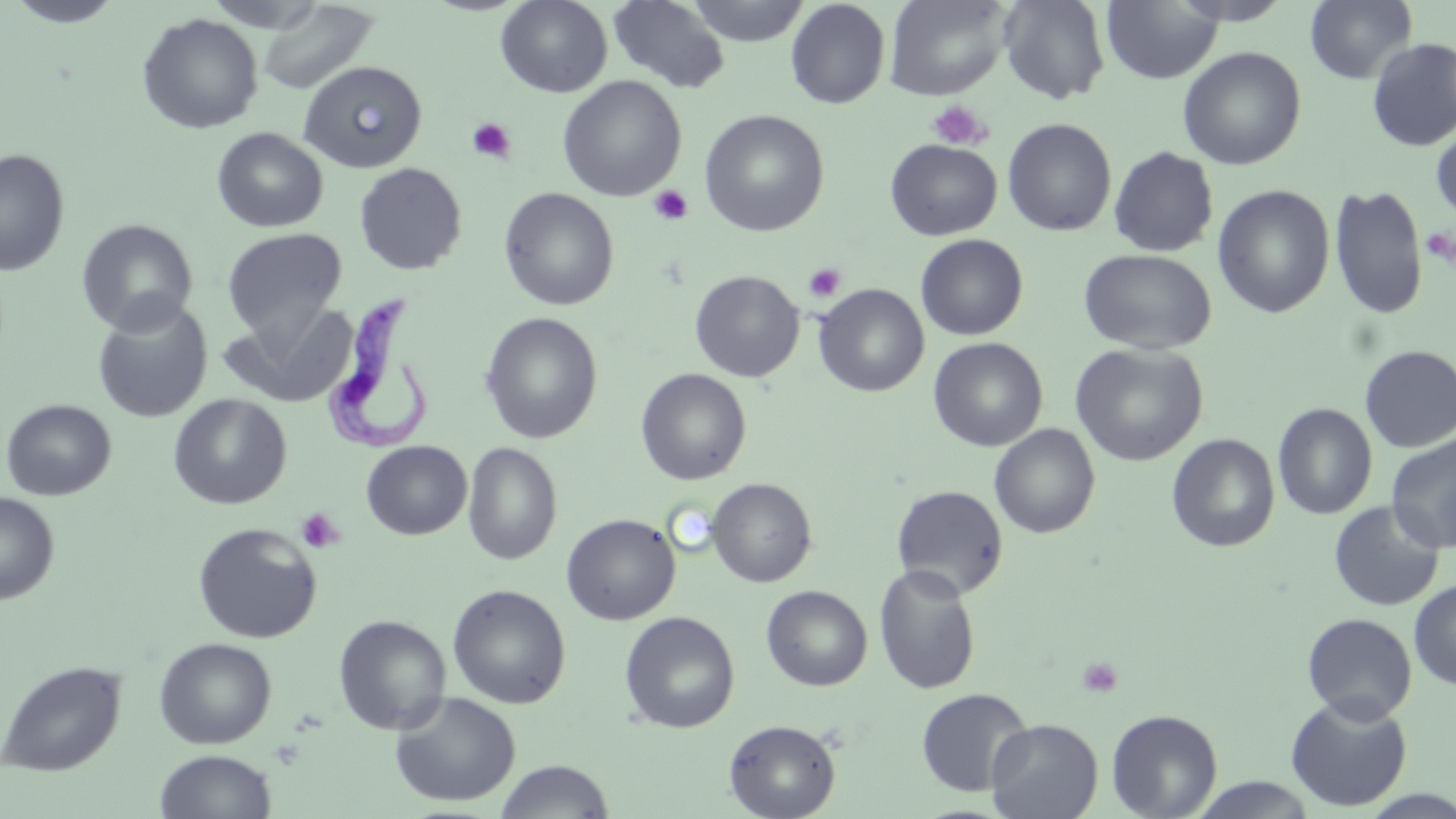
slide-level diagnosis = Trypanosoma brucei
uninfected red blood cell locations = approximate bounding boxes as (x1, y1, x2, y2) in pixels: (4, 0, 129, 28), (495, 0, 613, 98), (685, 0, 810, 46), (785, 0, 891, 109), (883, 0, 1012, 100), (997, 0, 1111, 105), (1101, 0, 1222, 84), (1303, 0, 1418, 85), (606, 1, 731, 94), (255, 2, 381, 96), (137, 13, 263, 134), (1366, 38, 1456, 152), (1177, 46, 1307, 170), (298, 61, 427, 173), (557, 75, 686, 202), (699, 109, 829, 237), (1002, 118, 1117, 236), (1430, 121, 1456, 225), (211, 127, 328, 232), (885, 139, 1002, 241), (1108, 146, 1219, 257), (0, 148, 70, 276), (354, 163, 467, 275), (1328, 183, 1428, 320), (1212, 185, 1335, 318), (498, 187, 619, 311), (76, 218, 198, 336), (221, 227, 347, 341), (915, 234, 1028, 340), (1078, 248, 1217, 355), (689, 270, 805, 382), (814, 284, 929, 397), (92, 298, 213, 423), (219, 300, 359, 409), (480, 312, 603, 444), (928, 337, 1048, 452), (1070, 342, 1209, 466), (1359, 344, 1456, 453), (635, 368, 752, 485), (169, 394, 292, 509), (1, 398, 117, 501), (1272, 402, 1378, 519), (989, 423, 1100, 539), (1166, 433, 1280, 553), (1386, 434, 1456, 553), (361, 441, 471, 540), (462, 442, 562, 566), (706, 478, 817, 587), (891, 484, 1009, 598), (0, 492, 59, 604), (1328, 500, 1446, 612), (561, 513, 680, 625), (192, 522, 323, 644), (873, 564, 981, 695), (1409, 580, 1456, 690), (447, 583, 571, 709), (761, 585, 872, 691), (619, 610, 740, 733), (1302, 613, 1417, 723), (333, 615, 452, 735), (154, 637, 277, 749), (0, 659, 127, 777), (915, 687, 1034, 796), (389, 692, 521, 808), (1285, 695, 1413, 812), (1105, 708, 1223, 819), (986, 717, 1103, 818), (724, 719, 841, 819), (154, 749, 277, 819), (494, 759, 615, 818), (1188, 777, 1319, 818)
Trypanosoma brucei locations = approximate bounding boxes as (x1, y1, x2, y2) in pixels: (315, 298, 435, 452)
field of view = single
platelet locations = approximate bounding boxes as (x1, y1, x2, y2) in pixels: (927, 100, 991, 151), (467, 117, 517, 163), (648, 185, 693, 226), (803, 262, 847, 303), (296, 507, 346, 552), (1077, 657, 1124, 698)
magnification = 1000x
stain = May-Grünwald-Giemsa
preparation = thin blood smear
image size = 1456×819 pixels
modality = light microscopy